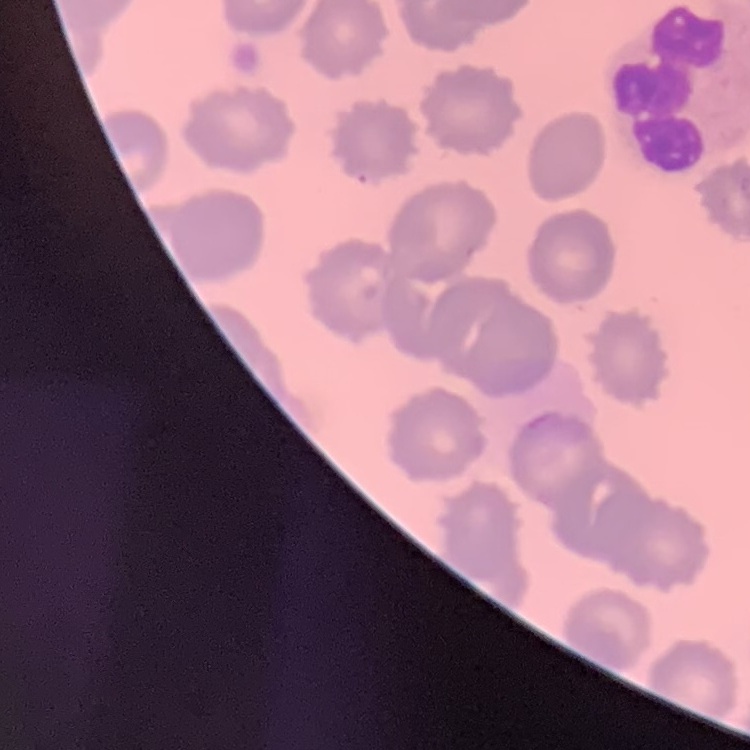 The red blood cells show no rouleaux formation. Thin blood film. One tile cut from a larger photomicrograph. Stained with either Field's or Giemsa.